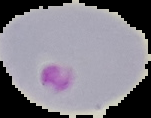

Summary:
  - Preparation: thin blood smear
  - Malaria status: parasitized
  - Image type: segmented cell region on a black background
  - Image size: 151×118 pixels